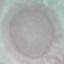
Malaria status: uninfected. Automatically extracted cell patch, resized to 64 × 64 pixels. Photographed with a smartphone camera at the microscope eyepiece. Giemsa stain. Thin blood smear.